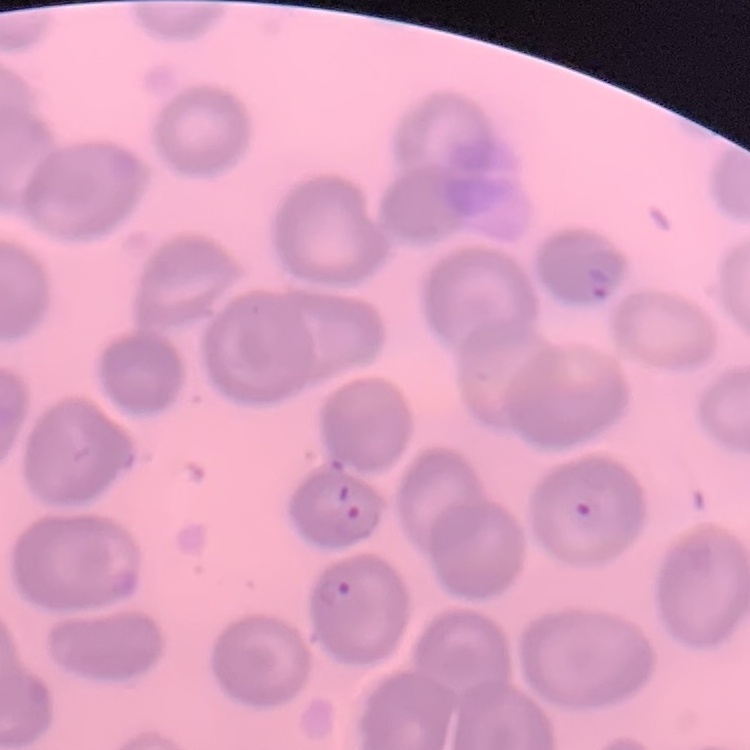

{
  "red_blood_cell_morphology": "no rouleaux formation",
  "stain": "Field's or Giemsa",
  "image_type": "square crop of a larger photomicrograph",
  "preparation": "thin peripheral smear"
}